Describe the morphology of the erythrocytes.
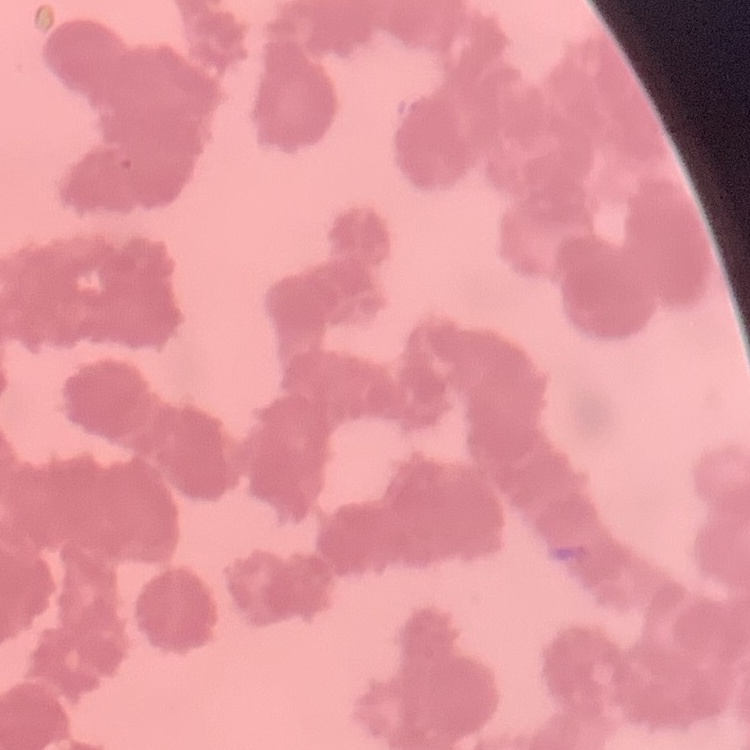

Rouleaux formation.

preparation: thin peripheral smear
stain: Field's or Giemsa
image_type: square crop of a larger photomicrograph